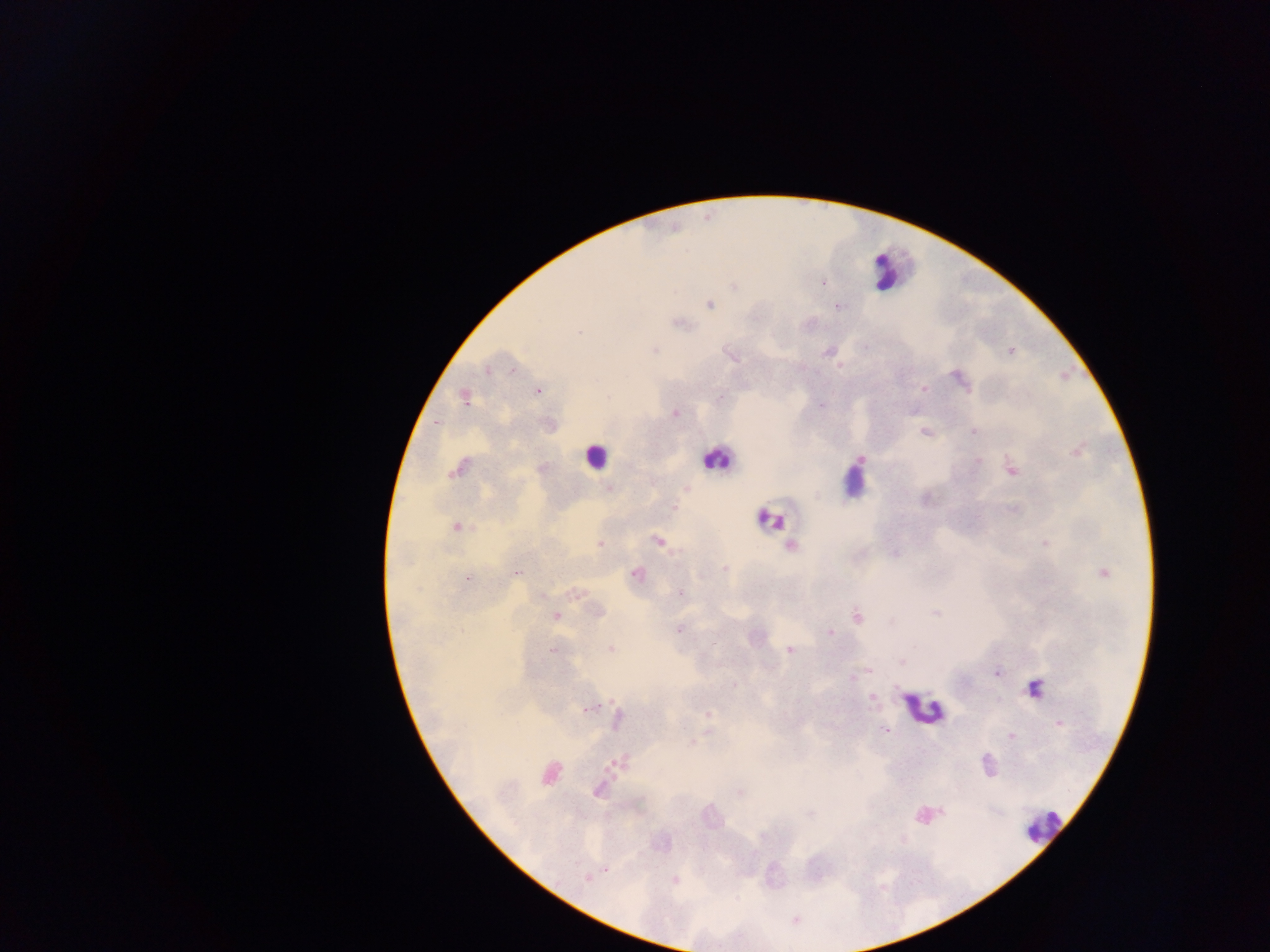
field of view = single
preparation = thick blood smear
malaria parasite locations = approximate centers as {x, y} in pixels: {823, 283}, {733, 287}, {710, 305}, {838, 307}, {680, 324}, {580, 332}, {655, 350}, {1010, 351}, {827, 352}, {731, 356}, {840, 366}, {487, 369}, {512, 370}, {959, 381}, {923, 389}, {538, 391}, {721, 397}, {465, 398}, {821, 405}, {675, 413}, {436, 421}, {924, 431}, {973, 431}, {1077, 450}, {861, 459}, {978, 461}, {459, 468}, {1011, 469}, {609, 488}, {687, 489}, {674, 507}, {1013, 509}, {456, 526}, {658, 541}, {1045, 543}, {600, 544}, {791, 545}, {893, 554}, {724, 569}, {518, 572}, {1104, 573}, {636, 574}, {468, 578}, {681, 593}, {575, 594}, {541, 596}, {597, 611}, {935, 613}, {556, 616}, {857, 616}, {679, 630}, {831, 633}, {714, 643}, {611, 649}, {552, 650}, {791, 650}, {902, 662}, {869, 670}, {997, 672}, {852, 676}, {1034, 689}, {872, 698}, {588, 708}, {709, 714}, {617, 719}, {1060, 724}, {885, 730}, {708, 732}, {1011, 736}, {692, 744}, {616, 763}, {986, 763}, {549, 773}, {598, 791}, {740, 792}, {941, 811}, {607, 870}, {586, 879}, {674, 880}
leukocyte locations = approximate centers as {x, y} in pixels: {890, 267}, {596, 456}, {716, 458}, {856, 483}, {770, 519}, {923, 709}, {1042, 826}
capture = mobile-phone photograph through a microscope
image size = 1270×952 pixels
country = Ghana